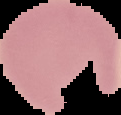
Malaria status: uninfected. Cell region segmented out of the field of view; the surrounding area is masked to black. Image is 121×115 pixels. From a thin blood smear.